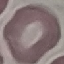
Summary:
  - Result: no malaria parasites seen
  - Stain: Giemsa
  - Preparation: thin blood smear
  - Image type: cell patch, automatically extracted from a larger field of view and resized to 64 × 64 pixels
  - Capture: smartphone camera at the microscope eyepiece